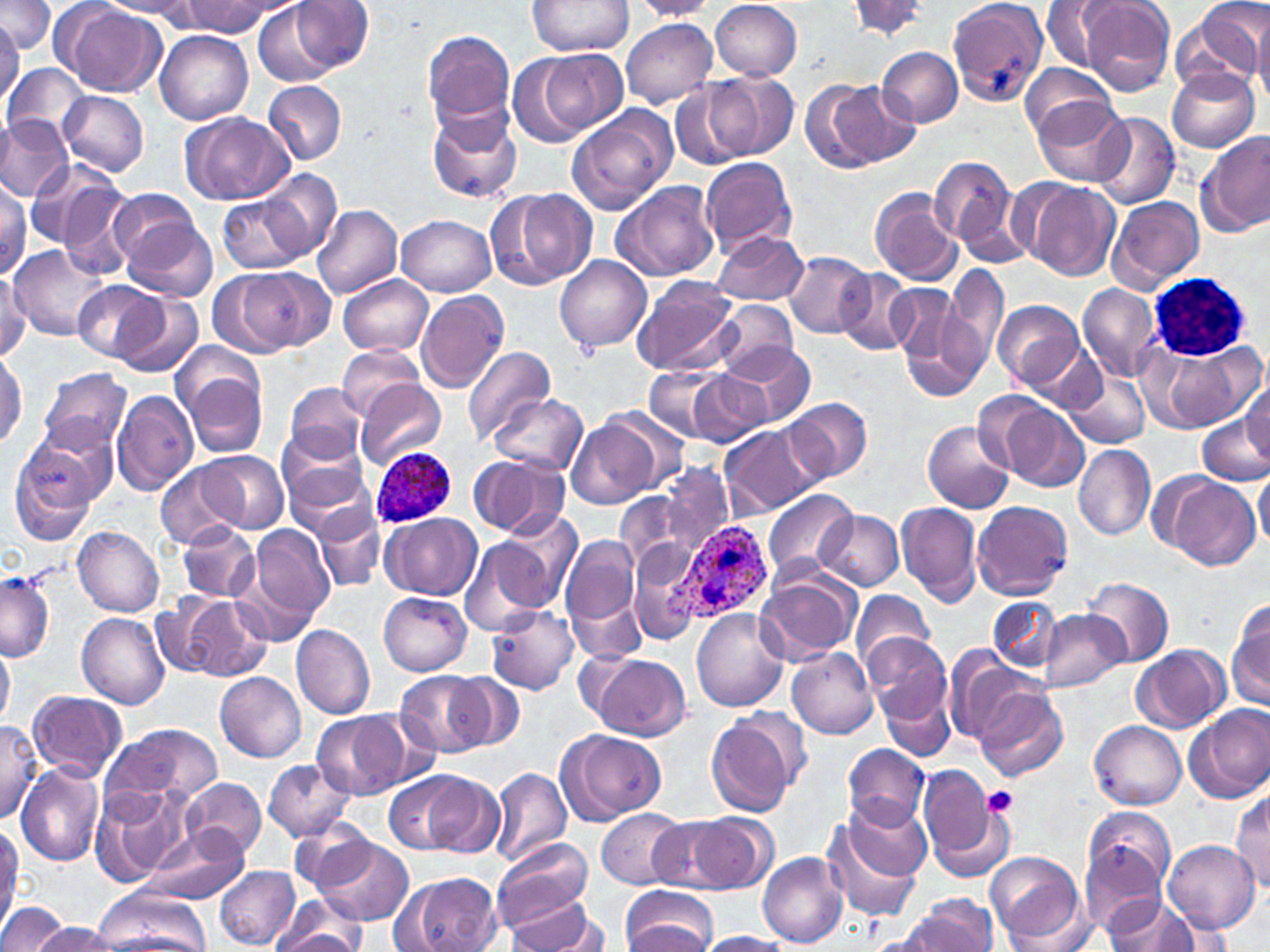
slide-level diagnosis = Plasmodium ovale
image size = 1270×952 pixels
uninfected red blood cell locations = approximate bounding boxes as (x1,y1)-(x2,y2) corner pairs in pixels: (100,0)-(202,17), (526,0)-(634,57), (711,0)-(803,80), (947,0)-(1049,106), (1040,0)-(1120,72), (1077,0)-(1176,96), (0,1)-(55,53), (178,1)-(273,35), (292,1)-(375,73), (629,1)-(720,20), (847,1)-(933,39), (254,2)-(340,86), (64,5)-(165,96), (1173,5)-(1263,96), (1253,8)-(1270,108), (622,19)-(718,108), (0,20)-(23,111), (422,29)-(515,129), (153,30)-(253,124), (877,45)-(963,128), (542,49)-(628,133), (508,54)-(596,149), (1020,62)-(1117,144), (2,63)-(90,145), (1167,68)-(1259,153), (704,70)-(796,161), (264,80)-(347,165), (671,80)-(752,171), (814,81)-(918,171), (59,90)-(149,176), (1030,97)-(1129,185), (426,105)-(521,203), (567,109)-(675,214), (1089,111)-(1181,210), (181,112)-(293,206), (0,116)-(72,202), (1199,132)-(1270,237), (928,154)-(1026,259), (701,156)-(798,257), (25,159)-(126,249), (258,169)-(343,260), (1016,178)-(1120,281), (0,179)-(29,280), (611,180)-(720,283), (58,184)-(137,282), (493,187)-(598,289), (109,188)-(205,270), (871,188)-(963,286), (218,193)-(311,275), (1108,195)-(1205,292), (312,201)-(403,299), (397,215)-(497,296), (122,217)-(217,303), (713,230)-(807,305), (8,246)-(108,340), (783,251)-(875,339), (555,255)-(651,354), (947,261)-(1010,365), (214,269)-(327,355), (836,269)-(914,355), (0,273)-(31,363), (339,275)-(433,357), (632,277)-(739,377), (73,279)-(165,363), (890,283)-(981,395), (1078,284)-(1162,381), (114,292)-(203,378), (416,292)-(509,392), (713,299)-(798,380), (993,300)-(1084,390), (171,342)-(265,427), (727,342)-(816,428), (462,343)-(557,444), (1141,344)-(1247,434), (0,346)-(27,449), (338,347)-(423,419), (645,365)-(729,441), (39,367)-(132,455), (1063,369)-(1149,448), (682,371)-(773,447), (185,372)-(266,459), (357,377)-(447,471), (282,380)-(369,464), (1242,383)-(1270,462), (113,390)-(198,496), (489,393)-(587,476), (786,398)-(872,483), (994,400)-(1089,492), (596,409)-(692,496), (1198,413)-(1269,486), (569,419)-(659,510), (923,420)-(1016,514), (720,426)-(811,516), (277,432)-(368,517), (8,439)-(103,545), (1073,443)-(1156,540), (202,451)-(289,533), (469,455)-(558,538), (155,462)-(240,547), (658,464)-(732,556), (1254,469)-(1270,553), (293,473)-(382,573), (1166,476)-(1260,569), (763,489)-(859,586), (971,499)-(1074,599), (896,502)-(982,606), (313,508)-(387,592), (815,509)-(904,590), (382,514)-(481,599), (488,519)-(580,616), (177,523)-(260,603), (249,524)-(336,626), (73,526)-(165,617), (561,533)-(642,640), (458,538)-(553,635), (629,546)-(700,648), (757,571)-(861,663), (0,573)-(55,662), (1084,576)-(1173,668), (851,590)-(933,673), (378,592)-(472,675), (171,594)-(270,681), (988,597)-(1061,673), (1229,600)-(1270,711), (486,604)-(578,695), (691,608)-(788,712), (1039,609)-(1127,693), (76,613)-(170,708), (291,623)-(375,720), (867,635)-(956,738), (0,636)-(14,731), (1134,644)-(1231,733), (785,647)-(878,739), (945,649)-(1037,747), (588,654)-(691,740), (397,670)-(490,758), (446,671)-(526,752), (215,672)-(306,763), (884,686)-(953,759), (975,687)-(1068,783), (26,690)-(126,780), (1184,704)-(1270,802), (313,710)-(406,800), (707,712)-(801,817), (358,713)-(440,793), (0,719)-(43,824), (1090,719)-(1187,809), (102,723)-(223,808), (558,729)-(665,824), (843,743)-(929,830), (263,758)-(355,841), (15,764)-(104,866), (489,766)-(573,868), (920,772)-(1004,876), (385,773)-(468,852), (422,773)-(504,856), (181,777)-(266,860), (90,784)-(192,887), (1230,789)-(1270,892), (844,797)-(932,879), (1084,805)-(1176,895), (820,806)-(925,925), (597,808)-(687,889), (687,812)-(777,894), (288,815)-(376,891), (650,817)-(739,891), (143,825)-(249,905), (306,834)-(413,926), (492,836)-(593,934), (1163,837)-(1260,934), (1078,839)-(1167,940), (0,843)-(22,932), (757,851)-(847,948), (986,851)-(1084,942), (215,866)-(301,949), (390,870)-(504,952), (621,886)-(718,952), (91,888)-(212,952), (270,896)-(369,952), (906,896)-(998,952), (1104,897)-(1205,952), (507,898)-(608,952), (0,902)-(69,952), (1006,904)-(1099,952), (31,922)-(121,952), (265,926)-(369,951), (866,930)-(944,952), (696,931)-(790,951)
field of view = single
magnification = 1000x
modality = light microscopy
platelet locations = approximate bounding boxes as (x1,y1)-(x2,y2) corner pairs in pixels: (983,786)-(1018,816)
Plasmodium ovale-infected red blood cell locations = approximate bounding boxes as (x1,y1)-(x2,y2) corner pairs in pixels: (369,446)-(458,527), (675,521)-(773,623)
preparation = thin blood film
white blood cell locations = approximate bounding boxes as (x1,y1)-(x2,y2) corner pairs in pixels: (1150,273)-(1252,360)
stain = May-Grünwald-Giemsa